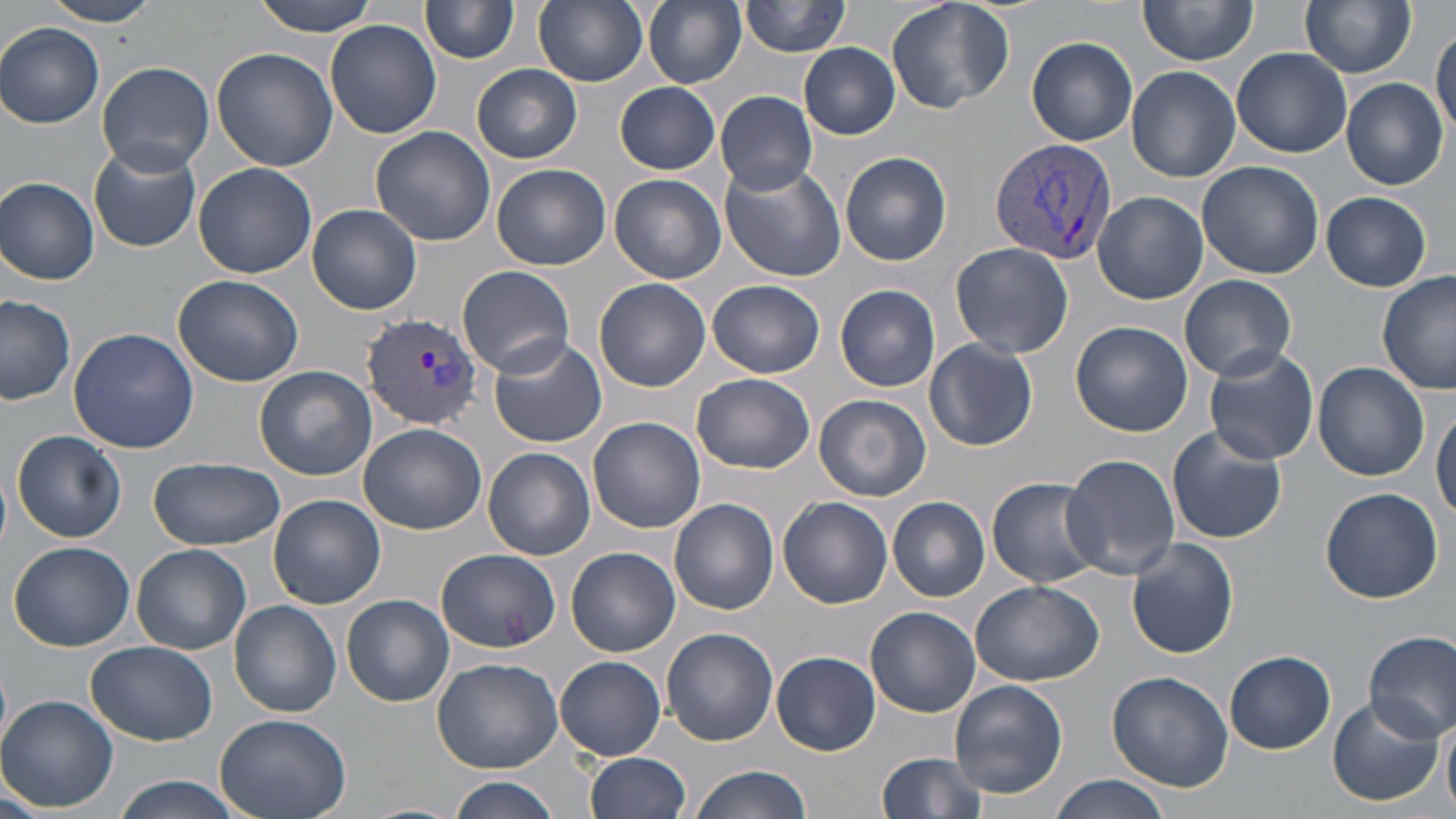
Summary:
  - Coordinate format: approximate bounding boxes as [x1, y1, x2, y2] in pixels
  - Plasmodium vivax-infected red blood cell locations: [989, 136, 1117, 267], [361, 313, 483, 427]
  - Uninfected red blood cell locations: [40, 0, 162, 26], [252, 0, 379, 36], [534, 0, 648, 87], [643, 0, 747, 87], [742, 0, 850, 57], [884, 0, 1014, 115], [1139, 0, 1257, 67], [1300, 0, 1417, 77], [419, 1, 520, 65], [324, 19, 441, 138], [0, 23, 104, 128], [1431, 24, 1455, 141], [1028, 37, 1138, 144], [798, 43, 900, 138], [1232, 47, 1352, 158], [213, 48, 340, 173], [95, 62, 214, 175], [472, 64, 582, 163], [1125, 65, 1243, 182], [1341, 77, 1447, 190], [615, 81, 721, 174], [716, 90, 818, 196], [369, 126, 495, 247], [89, 143, 203, 253], [841, 151, 952, 266], [718, 160, 846, 282], [1196, 160, 1325, 279], [191, 164, 318, 280], [492, 164, 611, 271], [610, 173, 726, 283], [1, 177, 100, 283], [1094, 191, 1207, 304], [1322, 191, 1432, 290], [307, 204, 421, 314], [950, 242, 1073, 358], [457, 265, 575, 378], [173, 273, 304, 387], [1376, 273, 1454, 395], [1178, 274, 1296, 383], [593, 278, 711, 392], [706, 279, 824, 378], [835, 284, 940, 390], [0, 294, 75, 404], [1070, 321, 1193, 437], [69, 328, 198, 453], [490, 338, 607, 448], [924, 339, 1038, 451], [1203, 346, 1319, 467], [1314, 361, 1429, 481], [255, 365, 377, 480], [693, 373, 817, 473], [812, 393, 933, 503], [1431, 401, 1456, 525], [587, 416, 705, 533], [358, 424, 487, 534], [1167, 426, 1286, 544], [12, 429, 127, 543], [484, 447, 595, 561], [1059, 453, 1179, 579], [149, 456, 286, 551], [987, 476, 1106, 587], [1319, 487, 1443, 605], [267, 494, 385, 610], [778, 496, 892, 610], [888, 496, 990, 601], [670, 498, 779, 613], [1127, 539, 1238, 660], [8, 541, 135, 651], [133, 545, 250, 655], [567, 548, 680, 656], [437, 549, 559, 651], [971, 579, 1102, 687], [343, 595, 453, 708], [862, 597, 1097, 705], [229, 599, 341, 717], [864, 607, 980, 717], [662, 628, 778, 747], [1365, 631, 1455, 740], [86, 640, 217, 745], [772, 651, 881, 753], [1225, 652, 1336, 753], [556, 656, 667, 759], [431, 657, 565, 772], [1106, 671, 1234, 791], [949, 680, 1067, 798], [0, 695, 117, 811], [1326, 696, 1442, 806], [1441, 709, 1456, 818], [214, 712, 351, 819], [587, 752, 692, 818], [875, 752, 988, 819], [690, 765, 809, 819], [1049, 774, 1171, 819], [113, 776, 243, 819], [447, 776, 560, 819], [0, 785, 47, 819], [356, 802, 466, 819]
  - Slide-level diagnosis: Plasmodium vivax
  - Preparation: thin blood smear
  - Image size: 1456×819 pixels
  - Magnification: 1000x
  - Stain: May-Grünwald-Giemsa
  - Field of view: one of a larger specimen
  - Modality: light microscopy